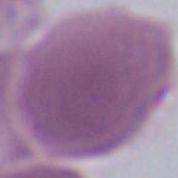

Summary:
  - Identification: erythrocyte
  - Magnification: 1000x
  - Modality: photomicrograph